Identify the cell.
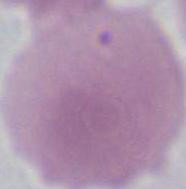
An erythrocyte.

Captured at 1000x magnification. Micrograph.